Outline each Plasmodium falciparum-infected red blood cell.
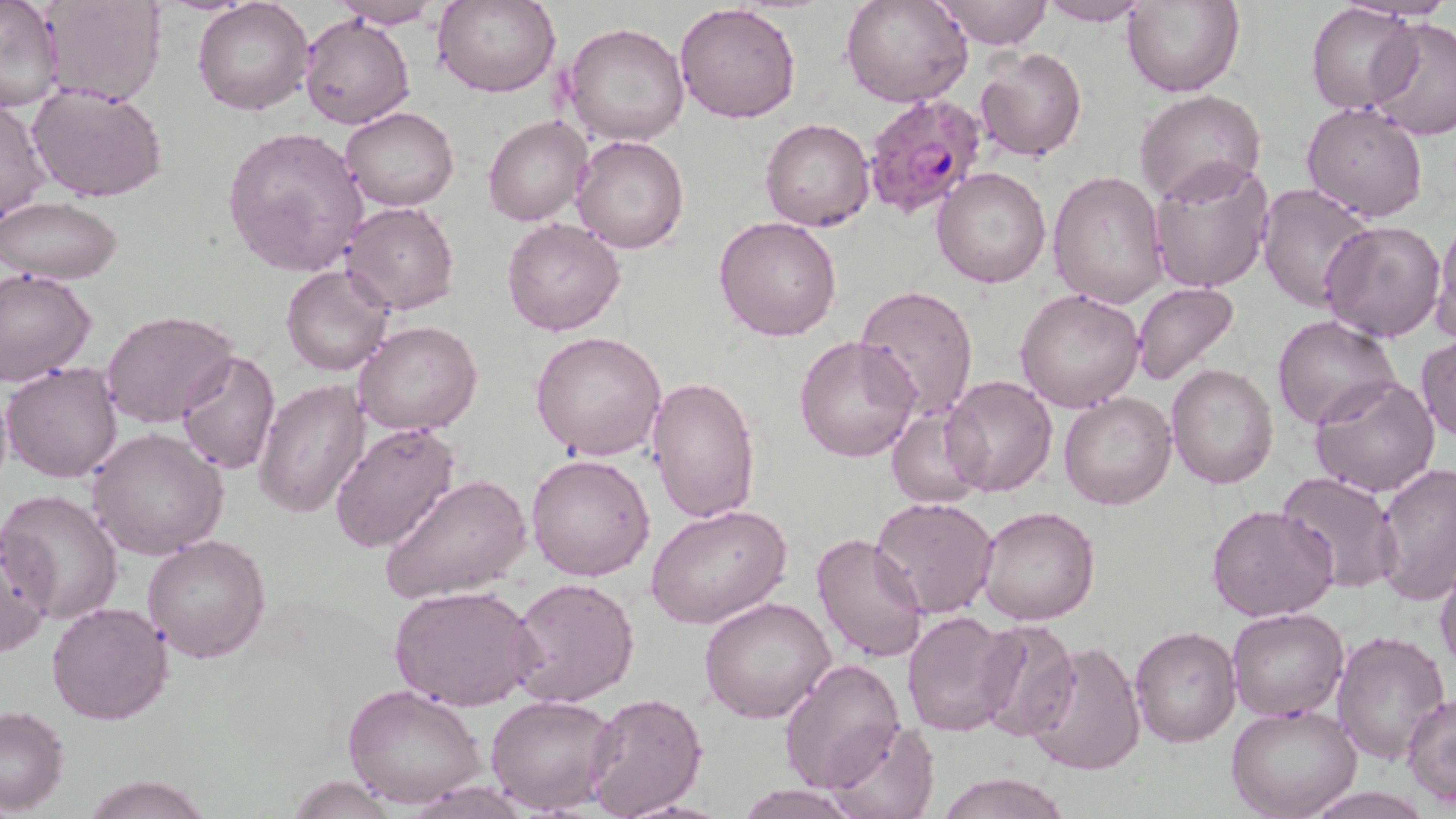

Approximate bounding boxes as (x1,y1)-(x2,y2) corner pairs in pixels.
Plasmodium falciparum-infected red blood cells: (859,92)-(988,222).

Summary:
  - Uninfected red blood cell locations: (0,0)-(66,113), (37,0)-(166,105), (434,0)-(561,98), (842,0)-(973,109), (937,0)-(1053,49), (192,1)-(312,116), (331,1)-(443,28), (1036,1)-(1155,26), (1123,1)-(1245,98), (674,2)-(801,124), (1308,3)-(1417,114), (300,14)-(414,130), (1366,17)-(1456,141), (564,23)-(690,147), (975,47)-(1087,162), (27,83)-(169,204), (1135,90)-(1266,209), (0,96)-(50,224), (1302,102)-(1429,221), (340,106)-(459,212), (482,114)-(591,227), (759,118)-(875,233), (222,126)-(370,275), (571,135)-(689,255), (1147,158)-(1275,293), (932,167)-(1052,289), (1049,169)-(1168,308), (1258,183)-(1379,312), (1,197)-(124,285), (341,202)-(459,315), (715,215)-(841,341), (1431,216)-(1456,344), (502,217)-(626,336), (1321,220)-(1446,342), (280,264)-(393,377), (0,270)-(96,385), (856,284)-(978,419), (1131,284)-(1241,387), (1014,289)-(1146,412), (100,310)-(240,427), (1273,315)-(1402,432), (354,319)-(484,438), (531,330)-(667,462), (795,334)-(921,462), (1416,337)-(1456,441), (176,352)-(281,474), (1,361)-(124,483), (1165,364)-(1279,490), (1309,374)-(1440,497), (942,375)-(1058,497), (0,376)-(13,499), (644,377)-(760,524), (254,379)-(369,517), (1059,391)-(1177,511), (885,408)-(986,508), (328,421)-(462,555), (86,426)-(230,559), (526,453)-(656,581), (1374,462)-(1456,604), (1276,471)-(1401,592), (379,474)-(531,605), (2,488)-(124,626), (870,496)-(998,619), (645,503)-(792,630), (1206,504)-(1339,623), (976,505)-(1101,626), (0,528)-(52,659), (810,532)-(929,664), (144,534)-(273,662), (1434,556)-(1456,679), (508,575)-(639,708), (389,585)-(538,713), (699,596)-(838,724), (46,602)-(173,726), (1226,607)-(1348,722), (901,610)-(1018,737), (1225,619)-(1450,741), (973,620)-(1081,740), (1129,626)-(1241,747), (1333,629)-(1451,763), (1023,641)-(1146,776), (779,657)-(908,793), (344,685)-(486,809), (581,692)-(708,818), (486,693)-(619,814), (1404,694)-(1456,805), (1227,704)-(1362,819), (0,705)-(70,814), (826,718)-(942,819), (933,772)-(1072,818), (80,775)-(213,819), (285,776)-(400,817), (733,786)-(858,818)
  - Slide-level diagnosis: Plasmodium falciparum
  - Field of view: single
  - Modality: light microscopy
  - Preparation: thin blood film
  - Magnification: 1000x
  - Stain: May-Grünwald-Giemsa
  - Image size: 1456×819 pixels